State which parasite is depicted.
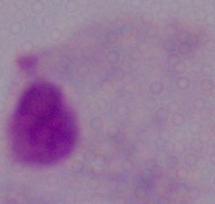

A trichomonad.

magnification = 1000x
modality = micrograph